Assess this cell for malaria.
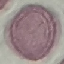
It is uninfected.

Summary:
  - Capture: smartphone camera at the microscope eyepiece
  - Image type: cell patch, automatically extracted from a larger field of view and resized to 64 × 64 pixels
  - Preparation: thin blood film
  - Stain: Giemsa